State the blood parasite species.
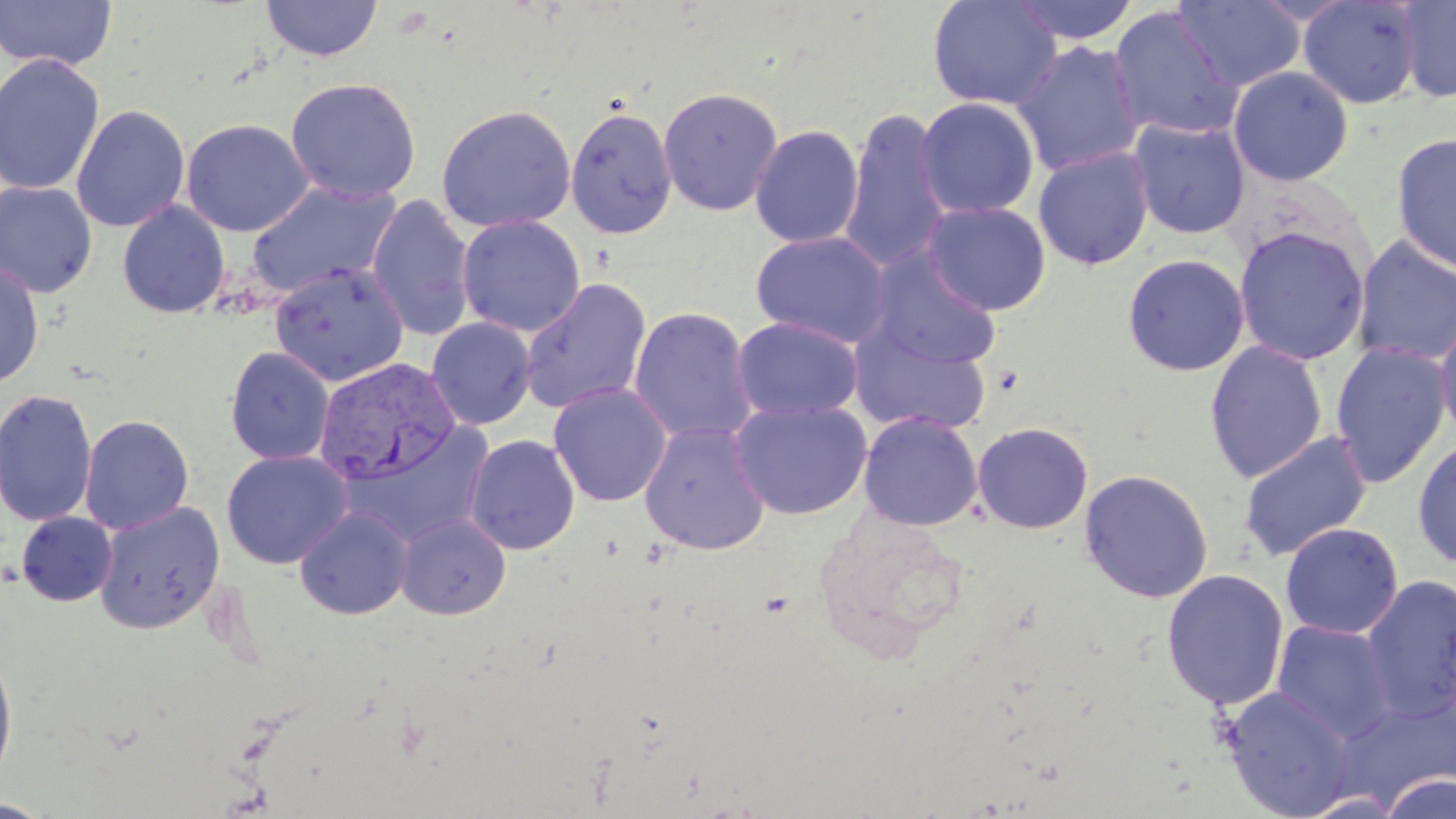

Plasmodium vivax.

Approximate bounding boxes as [x1, y1, x2, y2] in pixels. Uninfected red blood cell locations: [927, 0, 1062, 111], [1008, 0, 1139, 45], [1174, 0, 1305, 91], [1297, 0, 1423, 110], [1396, 0, 1456, 104], [0, 1, 117, 72], [261, 1, 383, 62], [1108, 5, 1244, 142], [1012, 40, 1146, 177], [0, 53, 105, 195], [1228, 65, 1354, 186], [285, 77, 422, 203], [658, 87, 783, 216], [915, 97, 1039, 219], [71, 104, 190, 233], [436, 104, 576, 233], [565, 105, 678, 240], [838, 108, 955, 273], [181, 118, 314, 237], [1128, 118, 1251, 239], [750, 124, 865, 249], [1390, 132, 1456, 274], [1033, 145, 1154, 270], [0, 181, 97, 298], [245, 181, 402, 299], [367, 194, 476, 342], [117, 200, 230, 319], [921, 201, 1051, 316], [457, 215, 585, 337], [1233, 226, 1370, 365], [750, 230, 891, 348], [1351, 234, 1456, 367], [867, 250, 1002, 370], [1122, 253, 1250, 376], [0, 258, 45, 389], [269, 263, 409, 386], [519, 277, 653, 415], [628, 306, 758, 446], [1434, 311, 1456, 450], [731, 317, 864, 423], [426, 318, 536, 430], [848, 324, 993, 437], [1204, 340, 1328, 483], [1330, 341, 1452, 488], [225, 347, 335, 465], [548, 383, 672, 507], [0, 389, 97, 528], [730, 398, 873, 520], [859, 412, 983, 531], [79, 414, 194, 535], [638, 421, 772, 555], [972, 422, 1093, 534], [345, 424, 495, 547], [1237, 429, 1373, 561], [464, 434, 580, 555], [1412, 437, 1456, 569], [221, 450, 353, 569], [1079, 469, 1214, 603], [93, 501, 225, 634], [294, 506, 413, 619], [16, 512, 117, 606], [395, 513, 510, 620], [1280, 522, 1404, 639], [1161, 568, 1289, 710], [1360, 575, 1456, 722], [1272, 621, 1396, 742], [0, 648, 17, 788], [1221, 686, 1357, 819], [1380, 772, 1456, 819], [0, 798, 53, 818]. Plasmodium vivax-infected red blood cell locations: [314, 358, 460, 486]. Image is 1456×819 pixels. One field of a larger specimen. May-Grünwald-Giemsa-stained preparation. Light microscopy. Thin blood smear. Captured at 1000x magnification.